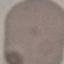

Summary:
  - Result: no malaria parasites seen
  - Preparation: thin smear
  - Image type: cell patch, automatically extracted from a larger field of view and resized to 64 × 64 pixels
  - Capture: smartphone through the microscope eyepiece
  - Stain: Giemsa